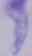 Captured at 1000x magnification. A trypanosome is shown. Photomicrograph.